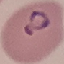

result: malaria parasites identified
stain: Giemsa
capture: smartphone through the microscope eyepiece
preparation: thin blood smear
image_type: cell patch, automatically extracted from a larger field of view and resized to 64 × 64 pixels